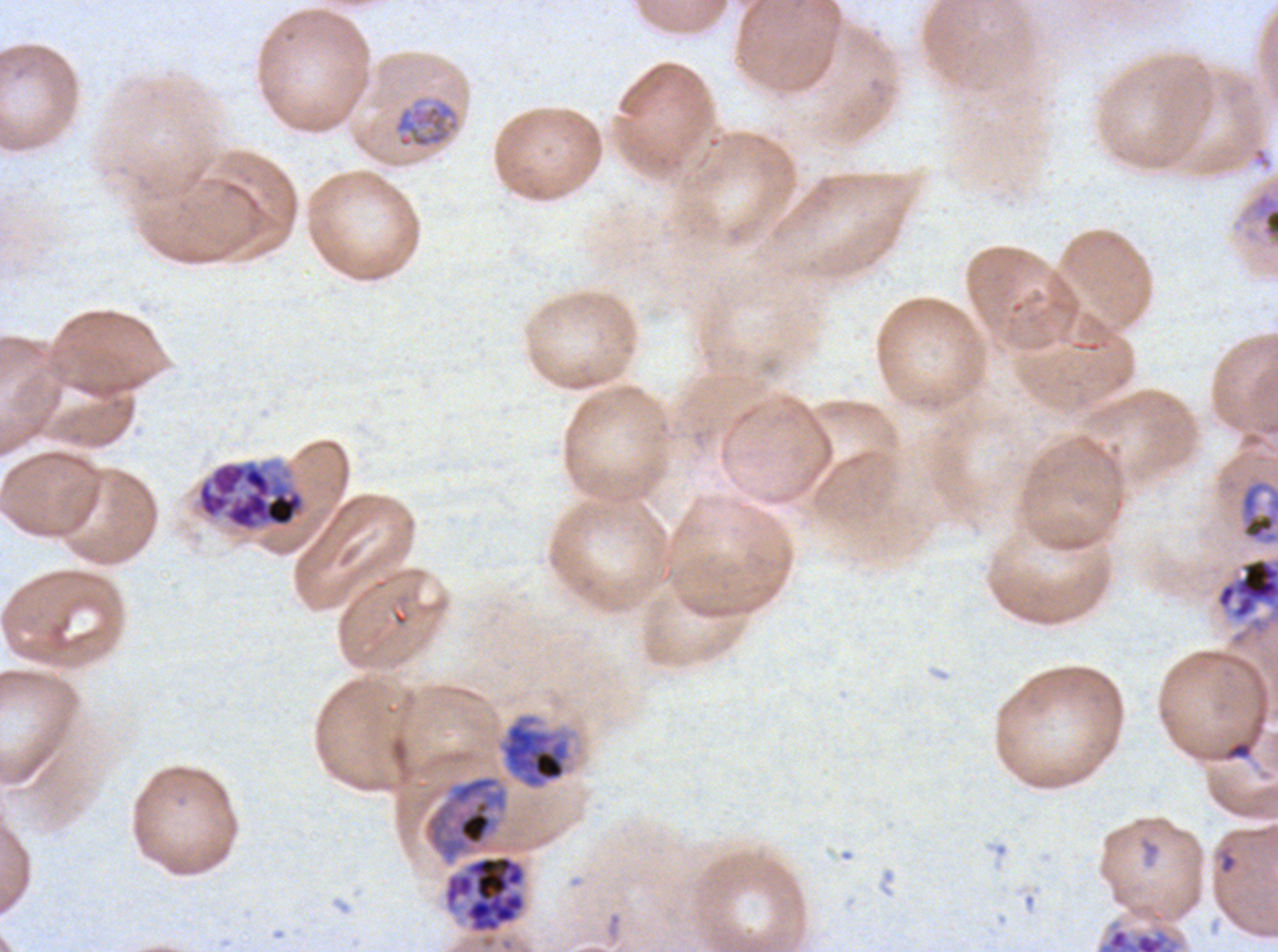
Approximate bounding boxes as (x1, y1, x2, y2) in pixels. Late schizont locations: (195, 458, 308, 533), (441, 853, 528, 935). Debris locations: (1240, 186, 1277, 250). Late trophozoite locations: (1215, 556, 1277, 621), (498, 713, 572, 790). Mid trophozoite locations: (392, 95, 461, 150), (1240, 480, 1277, 543). Early schizont locations: (424, 775, 509, 864), (1098, 927, 1181, 951). P. falciparum from a patient in The Gambia, cultured ex vivo for 24 to 48 hours. Image is 1278×952 pixels. A sub-image separated from a larger composite. Life-cycle stages observed: mid trophozoite, late trophozoite, early schizont, late schizont. Giemsa-stained preparation. Thin blood smear.